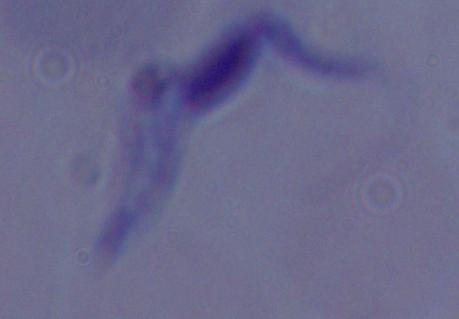

1000x magnification. Micrograph. A trypanosome is seen.